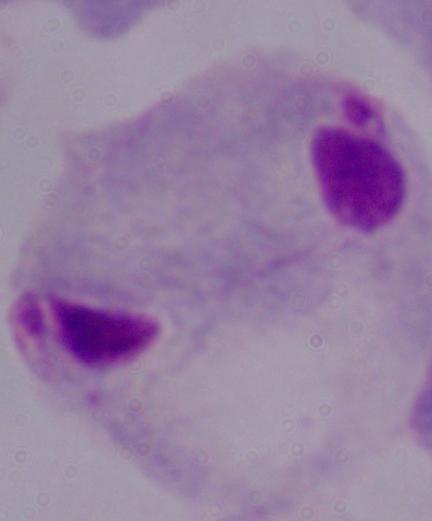 A trichomonad is shown. Photomicrograph. Captured at 1000x magnification.